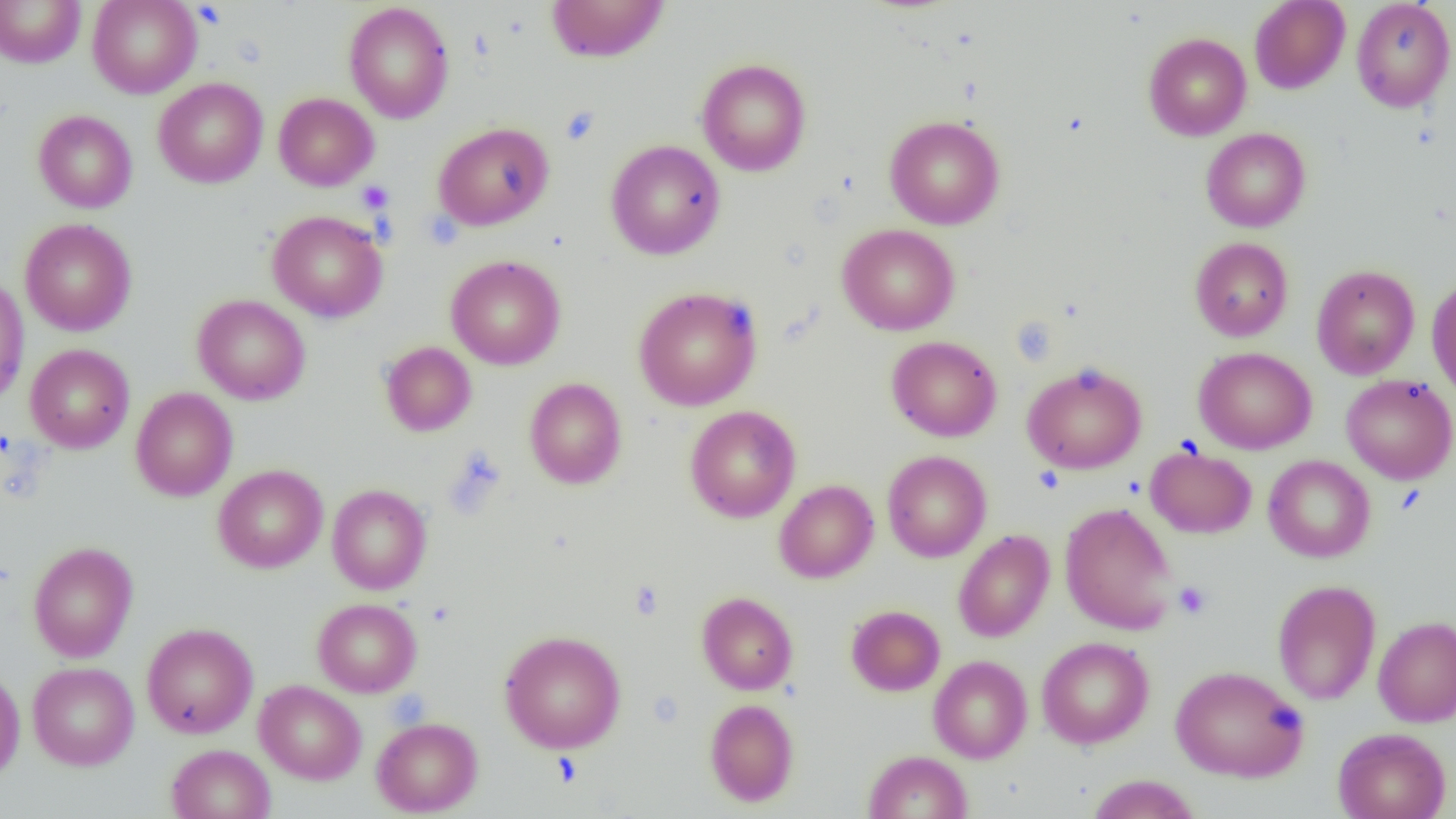 Approximate bounding boxes as named x1/y1/x2/y2 corners in pixels. Uninfected red blood cell locations: (x1=87, y1=0, x2=202, y2=98), (x1=546, y1=0, x2=669, y2=62), (x1=1249, y1=0, x2=1350, y2=94), (x1=1351, y1=0, x2=1455, y2=112), (x1=0, y1=1, x2=86, y2=68), (x1=343, y1=2, x2=454, y2=123), (x1=1143, y1=32, x2=1251, y2=140), (x1=696, y1=58, x2=811, y2=176), (x1=154, y1=77, x2=268, y2=188), (x1=274, y1=93, x2=379, y2=191), (x1=33, y1=109, x2=137, y2=213), (x1=885, y1=115, x2=1004, y2=230), (x1=433, y1=122, x2=554, y2=230), (x1=1201, y1=128, x2=1311, y2=232), (x1=606, y1=140, x2=725, y2=260), (x1=267, y1=210, x2=388, y2=322), (x1=20, y1=218, x2=137, y2=336), (x1=837, y1=223, x2=960, y2=335), (x1=1190, y1=237, x2=1293, y2=341), (x1=446, y1=255, x2=565, y2=370), (x1=1311, y1=264, x2=1420, y2=380), (x1=1427, y1=276, x2=1456, y2=402), (x1=0, y1=278, x2=29, y2=407), (x1=634, y1=286, x2=762, y2=411), (x1=192, y1=294, x2=310, y2=405), (x1=886, y1=335, x2=1002, y2=441), (x1=380, y1=341, x2=477, y2=436), (x1=25, y1=344, x2=134, y2=453), (x1=1194, y1=347, x2=1317, y2=454), (x1=1022, y1=362, x2=1147, y2=474), (x1=1341, y1=375, x2=1456, y2=485), (x1=525, y1=377, x2=627, y2=489), (x1=130, y1=387, x2=238, y2=501), (x1=685, y1=405, x2=800, y2=522), (x1=1146, y1=445, x2=1257, y2=538), (x1=882, y1=450, x2=991, y2=562), (x1=1263, y1=455, x2=1375, y2=562), (x1=213, y1=464, x2=327, y2=573), (x1=774, y1=479, x2=878, y2=583), (x1=327, y1=484, x2=431, y2=594), (x1=1060, y1=502, x2=1177, y2=635), (x1=953, y1=529, x2=1054, y2=642), (x1=27, y1=541, x2=138, y2=662), (x1=1272, y1=579, x2=1381, y2=705), (x1=697, y1=592, x2=798, y2=695), (x1=312, y1=598, x2=422, y2=697), (x1=847, y1=605, x2=944, y2=696), (x1=1373, y1=615, x2=1456, y2=727), (x1=141, y1=622, x2=258, y2=738), (x1=499, y1=630, x2=626, y2=753), (x1=1037, y1=636, x2=1154, y2=748), (x1=928, y1=655, x2=1033, y2=763), (x1=28, y1=661, x2=139, y2=770), (x1=1171, y1=665, x2=1308, y2=782), (x1=0, y1=666, x2=25, y2=781), (x1=254, y1=680, x2=366, y2=784), (x1=705, y1=698, x2=799, y2=806), (x1=372, y1=717, x2=483, y2=816), (x1=1333, y1=727, x2=1451, y2=819), (x1=166, y1=744, x2=275, y2=819), (x1=864, y1=750, x2=972, y2=818), (x1=1087, y1=774, x2=1202, y2=819). Platelet locations: (x1=193, y1=2, x2=227, y2=29), (x1=560, y1=106, x2=600, y2=145), (x1=356, y1=180, x2=395, y2=214), (x1=422, y1=211, x2=462, y2=250), (x1=629, y1=581, x2=665, y2=620), (x1=1173, y1=581, x2=1212, y2=620), (x1=552, y1=752, x2=582, y2=786). Slide-level diagnosis: no evidence of blood parasites. Image is 1456×819 pixels. One field of a larger specimen. Optical microscopy. Thin blood film. 1000x magnification.